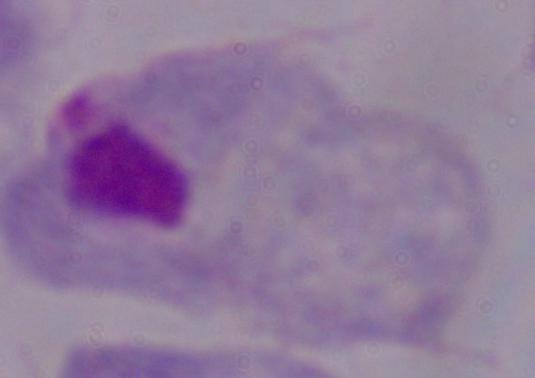
Summary:
  - Modality: micrograph
  - Identification: trichomonad
  - Magnification: 1000x